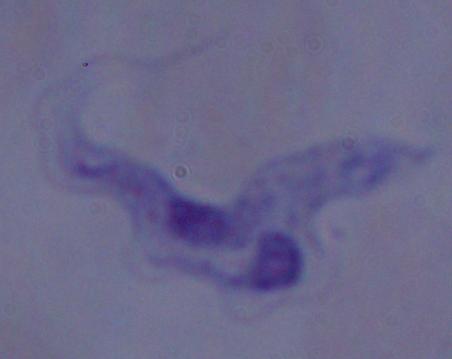
{
  "identification": "trypanosome",
  "modality": "photomicrograph",
  "magnification": "1000x"
}